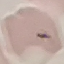 Result: no malaria parasites seen. Thin blood film. Giemsa stain. Automatically extracted cell patch, resized to 64 × 64 pixels. Photographed with a smartphone camera at the microscope eyepiece.